Locate every leukocyte (white blood cell).
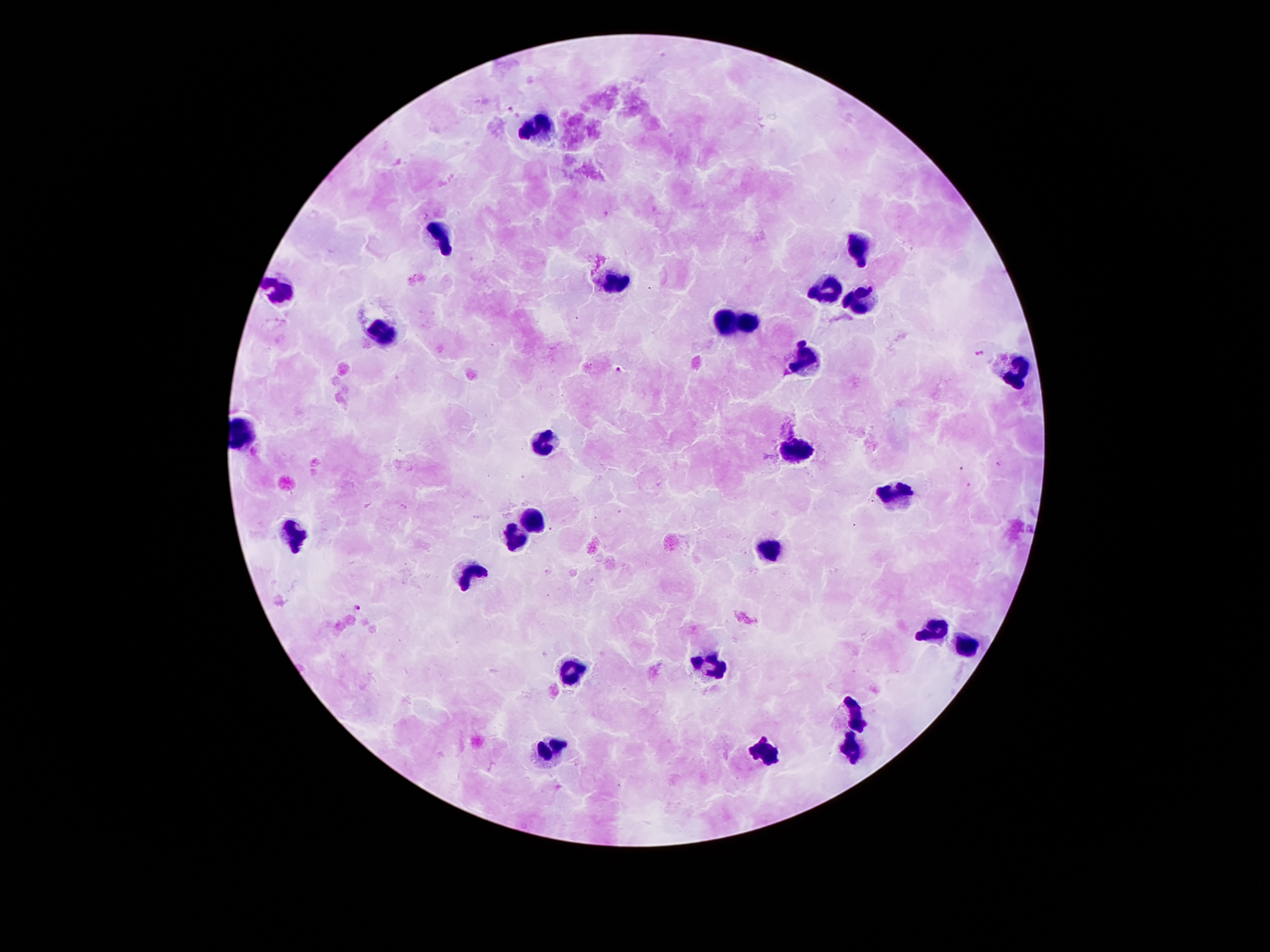
Approximate centers as (x, y) in pixels.
Leukocytes: (542, 131), (443, 239), (863, 247), (616, 279), (280, 291), (821, 296), (865, 299), (722, 321), (752, 323), (384, 331), (806, 358), (1019, 370), (547, 442), (796, 449), (890, 499), (534, 519), (295, 538), (517, 538), (767, 551), (465, 575), (937, 629), (967, 644), (712, 664), (571, 671), (856, 714), (853, 746), (547, 751), (764, 755).

Summary:
  - Plasmodium parasite locations: (511, 109), (982, 353), (620, 369), (357, 610)
  - Patient malaria status: infected with Plasmodium falciparum
  - Magnification: 100x
  - Field of view: one from this slide
  - Stain: Giemsa
  - Image size: 1270×952 pixels
  - Preparation: thick blood film
  - Capture: smartphone through the microscope eyepiece